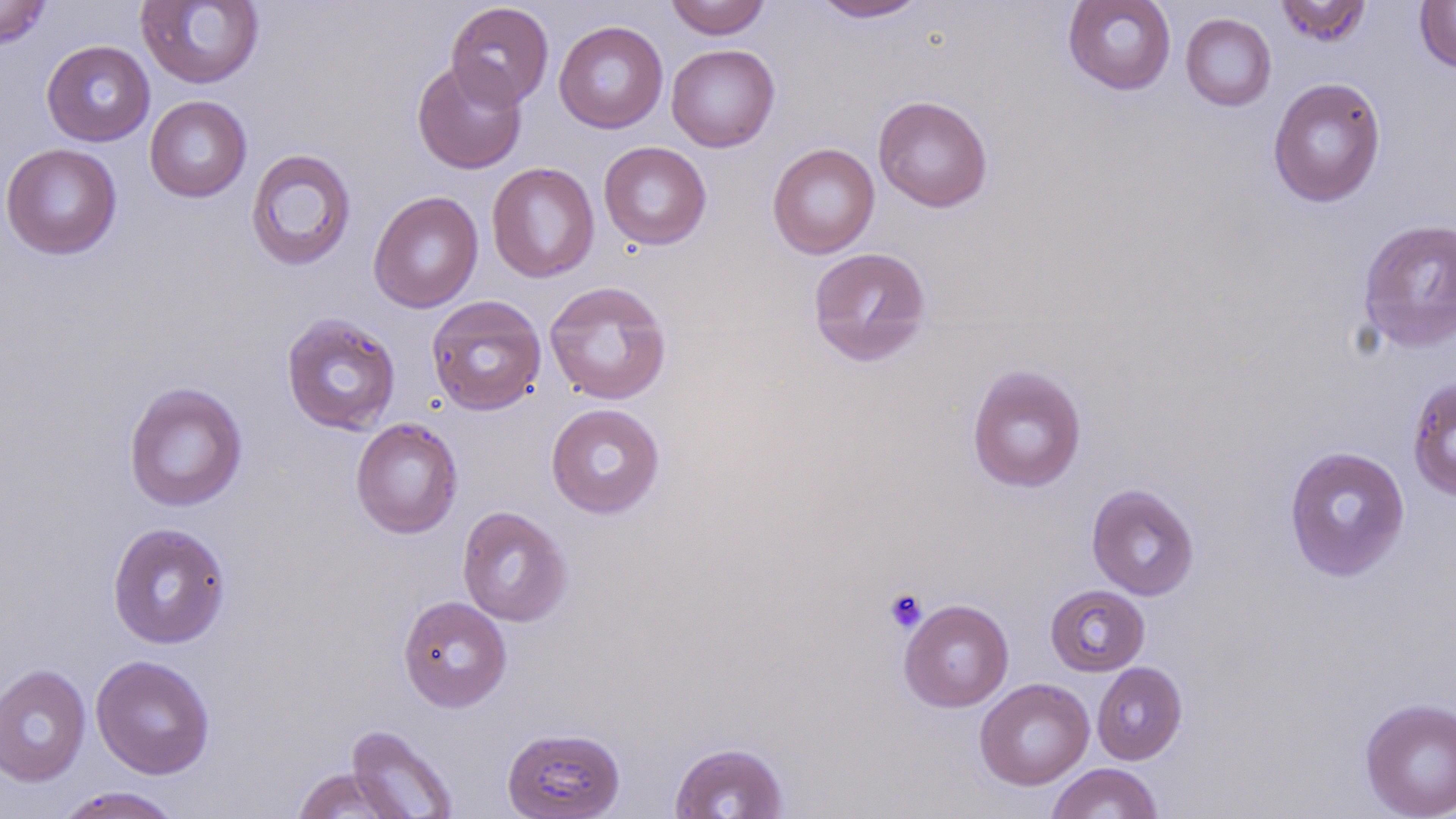

slide-level diagnosis = negative for blood parasites
uninfected red blood cell locations = approximate bounding boxes as [x1, y1, x2, y2] in pixels: [0, 0, 53, 49], [137, 0, 265, 89], [665, 0, 771, 40], [811, 0, 930, 23], [1063, 0, 1176, 95], [1275, 0, 1371, 47], [1414, 0, 1456, 73], [445, 2, 554, 109], [1180, 13, 1276, 111], [554, 20, 668, 134], [41, 40, 155, 146], [666, 44, 780, 152], [411, 59, 527, 174], [1268, 77, 1386, 208], [872, 95, 993, 212], [145, 96, 252, 203], [598, 141, 712, 250], [767, 142, 880, 259], [1, 143, 123, 260], [245, 148, 357, 271], [487, 162, 600, 283], [368, 191, 484, 314], [1357, 218, 1456, 353], [808, 246, 931, 366], [543, 280, 673, 405], [426, 295, 547, 416], [280, 313, 401, 435], [967, 364, 1087, 493], [1407, 375, 1456, 501], [123, 381, 248, 512], [546, 402, 665, 518], [350, 417, 464, 539], [1283, 446, 1411, 582], [1086, 483, 1199, 600], [457, 506, 574, 626], [107, 522, 232, 649], [1045, 584, 1149, 676], [397, 595, 513, 712], [899, 599, 1014, 712], [91, 654, 216, 779], [1091, 662, 1187, 765], [0, 664, 91, 788], [974, 678, 1094, 790], [1359, 698, 1456, 819], [345, 724, 459, 818], [502, 727, 626, 819], [669, 741, 790, 819], [1046, 763, 1163, 819], [291, 767, 408, 818], [52, 786, 186, 818]
stain = May-Grünwald-Giemsa
preparation = thin blood smear
image size = 1456×819 pixels
modality = optical microscopy
platelet locations = approximate bounding boxes as [x1, y1, x2, y2] in pixels: [883, 588, 927, 633]
field of view = single
magnification = 1000x